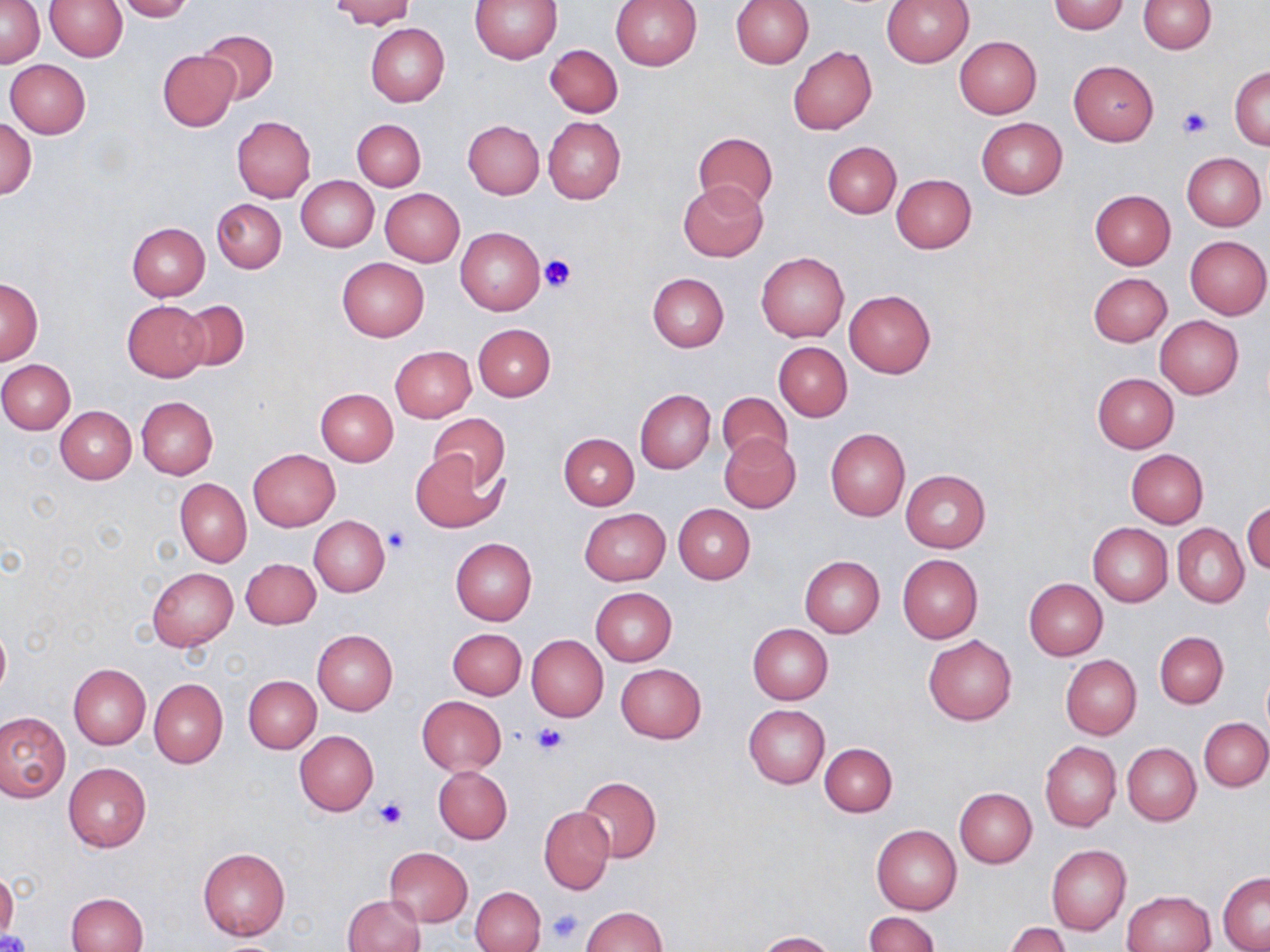
{
  "slide_level_diagnosis": "negative for blood parasites",
  "magnification": "1000x",
  "platelet_locations": "approximate bounding boxes as (x1, y1, x2, y2) in pixels: (1179, 107, 1211, 138), (539, 254, 577, 294), (382, 524, 413, 555), (532, 723, 570, 756), (375, 797, 409, 829), (547, 909, 586, 945), (0, 930, 30, 952)",
  "stain": "May-Grünwald-Giemsa",
  "field_of_view": "one of a larger specimen",
  "preparation": "thin blood smear",
  "image_size": "1270×952 pixels",
  "modality": "light microscopy",
  "uninfected_red_blood_cell_locations": "approximate bounding boxes as (x1, y1, x2, y2) in pixels: (2, 0, 43, 68), (114, 0, 195, 21), (328, 0, 416, 29), (471, 0, 561, 64), (880, 0, 975, 66), (1138, 0, 1217, 53), (44, 1, 127, 61), (609, 1, 702, 70), (731, 1, 813, 67), (1048, 1, 1131, 34), (366, 23, 450, 107), (198, 29, 278, 105), (954, 36, 1042, 118), (545, 43, 623, 118), (788, 46, 876, 135), (157, 49, 238, 130), (4, 59, 90, 138), (1068, 60, 1159, 146), (1230, 66, 1270, 149), (232, 116, 316, 201), (543, 117, 626, 203), (976, 117, 1067, 198), (0, 119, 37, 199), (352, 119, 425, 190), (463, 120, 544, 199), (693, 131, 777, 210), (823, 141, 900, 218), (1182, 152, 1266, 229), (891, 174, 976, 253), (295, 175, 378, 252), (678, 179, 769, 261), (380, 188, 465, 266), (1089, 189, 1175, 269), (213, 199, 287, 273), (127, 222, 210, 300), (455, 227, 546, 317), (1185, 235, 1269, 319), (756, 250, 849, 342), (338, 257, 428, 341), (1088, 272, 1172, 347), (646, 273, 728, 352), (0, 280, 43, 363), (844, 289, 935, 377), (177, 299, 248, 372), (122, 300, 209, 381), (1155, 316, 1244, 398), (472, 323, 555, 401), (775, 342, 852, 420), (390, 345, 476, 421), (0, 360, 76, 434), (1091, 373, 1179, 453), (316, 387, 398, 466), (635, 389, 716, 474), (717, 391, 794, 465), (136, 397, 218, 480), (56, 406, 135, 482), (428, 411, 509, 492), (826, 429, 910, 520), (719, 432, 801, 514), (558, 433, 639, 509), (248, 449, 340, 531), (1126, 449, 1208, 527), (411, 451, 504, 534), (901, 470, 991, 551), (176, 478, 251, 568), (1243, 500, 1270, 577), (673, 503, 755, 583), (579, 508, 670, 585), (309, 517, 390, 596), (1089, 523, 1172, 606), (1173, 524, 1249, 607), (451, 538, 537, 626), (897, 554, 982, 643), (800, 556, 885, 637), (242, 558, 321, 629), (148, 567, 237, 651), (1025, 578, 1108, 660), (590, 588, 677, 665), (0, 622, 10, 699), (748, 623, 833, 703), (447, 628, 526, 699), (311, 629, 397, 714), (1154, 631, 1228, 708), (527, 635, 608, 722), (924, 635, 1017, 725), (1061, 655, 1142, 739), (616, 663, 707, 743), (68, 664, 150, 749), (1262, 669, 1270, 739), (244, 676, 320, 753), (148, 679, 227, 768), (416, 695, 507, 775), (744, 705, 830, 789), (0, 712, 70, 801), (1200, 718, 1270, 790), (295, 730, 379, 816), (1039, 741, 1121, 833), (820, 743, 896, 817), (1123, 743, 1201, 825), (63, 762, 152, 852), (433, 765, 512, 844), (576, 777, 662, 863), (954, 787, 1037, 867), (539, 807, 614, 894), (872, 824, 962, 914), (1047, 845, 1131, 936), (198, 848, 290, 939), (384, 848, 472, 926), (1218, 873, 1270, 951), (471, 886, 546, 952), (1121, 890, 1216, 952), (66, 892, 147, 952), (342, 894, 425, 952), (581, 906, 668, 951), (864, 912, 939, 952), (1005, 923, 1071, 952), (755, 930, 837, 952)"
}